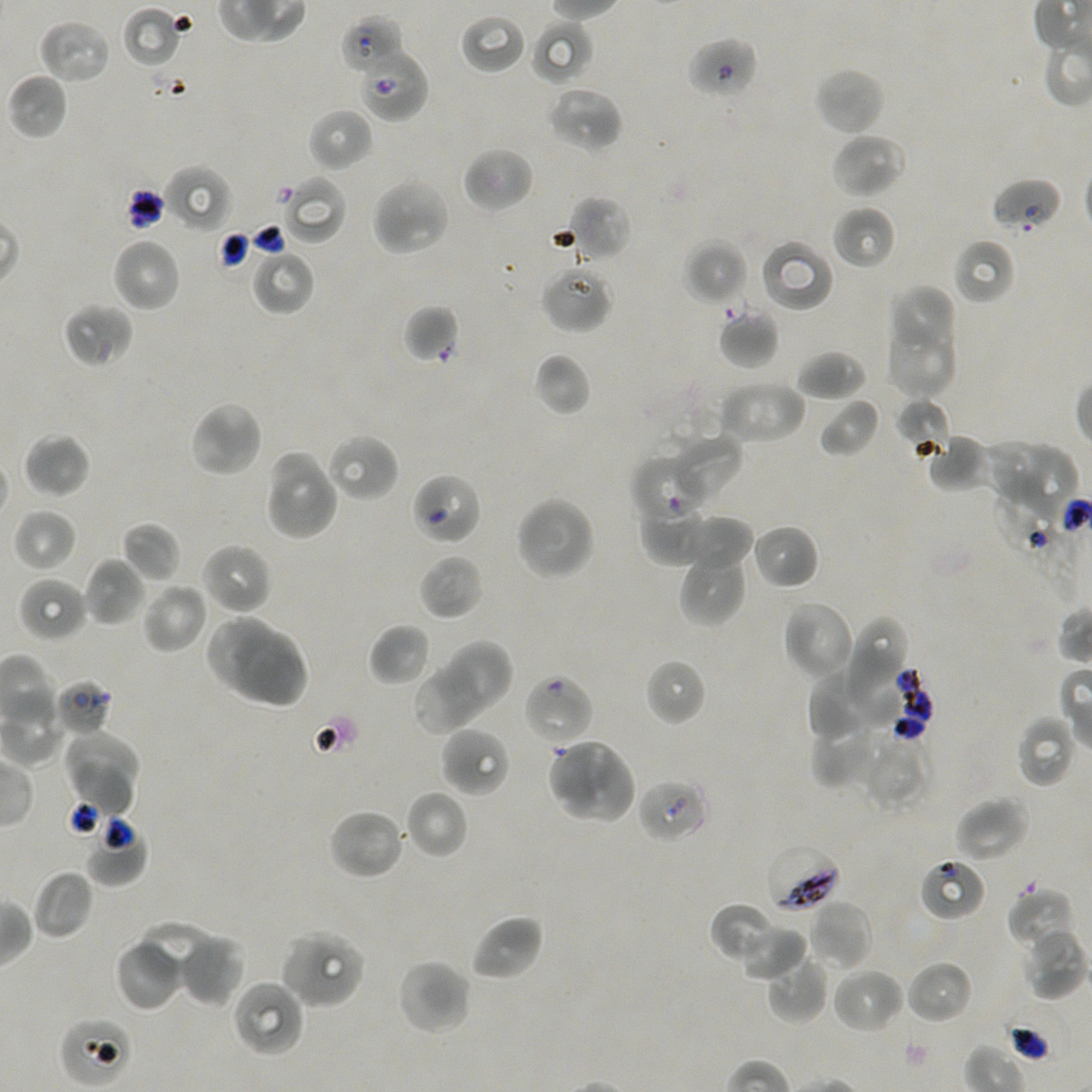

Approximate bounding boxes as [x1, y1, x2, y2] in pixels. Not every red blood cell is marked. A life-cycle stage — or a range of stages, where the recorded stages span more than one — follows each staged infected red blood cell.
Summary:
  - Locations of uninfected red blood cells: [122, 5, 184, 69], [459, 14, 527, 75], [38, 18, 113, 84], [531, 19, 594, 85], [814, 67, 886, 136], [7, 72, 68, 141], [546, 86, 623, 153], [308, 107, 374, 172], [830, 132, 905, 199], [462, 146, 534, 213], [164, 164, 232, 233], [283, 175, 348, 244], [371, 176, 451, 257], [568, 195, 631, 261], [831, 205, 896, 270], [111, 238, 181, 314], [759, 238, 835, 313], [951, 238, 1015, 306], [683, 240, 748, 307], [249, 249, 314, 315], [540, 264, 615, 333], [889, 285, 954, 348], [62, 302, 134, 368], [718, 306, 779, 369], [886, 316, 957, 397], [796, 350, 867, 401], [533, 352, 591, 416], [718, 379, 807, 445], [894, 396, 953, 456], [818, 397, 881, 458], [189, 401, 263, 479], [668, 431, 744, 505], [22, 432, 91, 498], [326, 433, 401, 503], [925, 434, 990, 492], [987, 441, 1079, 522], [273, 448, 329, 516], [266, 471, 338, 545], [514, 495, 597, 581], [12, 508, 77, 572], [639, 511, 712, 565], [679, 515, 753, 572], [122, 522, 181, 583], [751, 524, 819, 590], [200, 543, 272, 615], [678, 547, 747, 627], [418, 554, 485, 620], [83, 556, 147, 627], [19, 576, 88, 642], [141, 581, 209, 655], [782, 599, 856, 680], [206, 615, 279, 692], [845, 617, 909, 696], [369, 623, 432, 685], [232, 629, 308, 706], [441, 639, 514, 711], [843, 649, 908, 731], [644, 657, 706, 726], [414, 660, 490, 733], [809, 667, 875, 741], [1015, 712, 1077, 789], [811, 714, 879, 788], [440, 725, 510, 798], [62, 731, 141, 814], [860, 737, 930, 809], [546, 738, 638, 824], [404, 790, 468, 860], [953, 795, 1031, 862], [327, 807, 406, 881], [31, 868, 94, 940], [1007, 887, 1079, 953], [808, 899, 874, 970], [711, 903, 774, 960], [469, 913, 545, 981], [137, 922, 219, 982], [1020, 926, 1088, 1000], [278, 928, 366, 1010], [743, 930, 807, 980], [179, 932, 245, 1006], [115, 936, 184, 1013], [765, 953, 829, 1025], [398, 959, 471, 1035], [906, 960, 973, 1024], [831, 966, 905, 1034], [230, 979, 306, 1059]
  - Locations of red blood cells of indeterminate infection status: [687, 37, 758, 96], [991, 177, 1063, 235], [403, 305, 459, 363], [632, 454, 707, 528], [411, 471, 482, 545], [989, 477, 1064, 551], [524, 674, 594, 749], [54, 678, 113, 739], [74, 766, 131, 817], [636, 778, 708, 843], [82, 816, 149, 887], [919, 857, 987, 921], [1005, 1004, 1072, 1062], [59, 1016, 133, 1087]
  - Locations of infected red blood cells: [340, 15, 405, 73] late ring to early trophozoite; [356, 48, 428, 122] early ring to early trophozoite; [764, 843, 842, 915]
  - Objective: 100x, oil immersion, numerical aperture 1.45
  - Field of view: one from this slide
  - Donor blood group: A+/O+
  - Culture: in-vitro Plasmodium falciparum strain NF54, static
  - Image size: 1092×1092 pixels
  - Preparation: thin blood smear
  - Stain: Giemsa